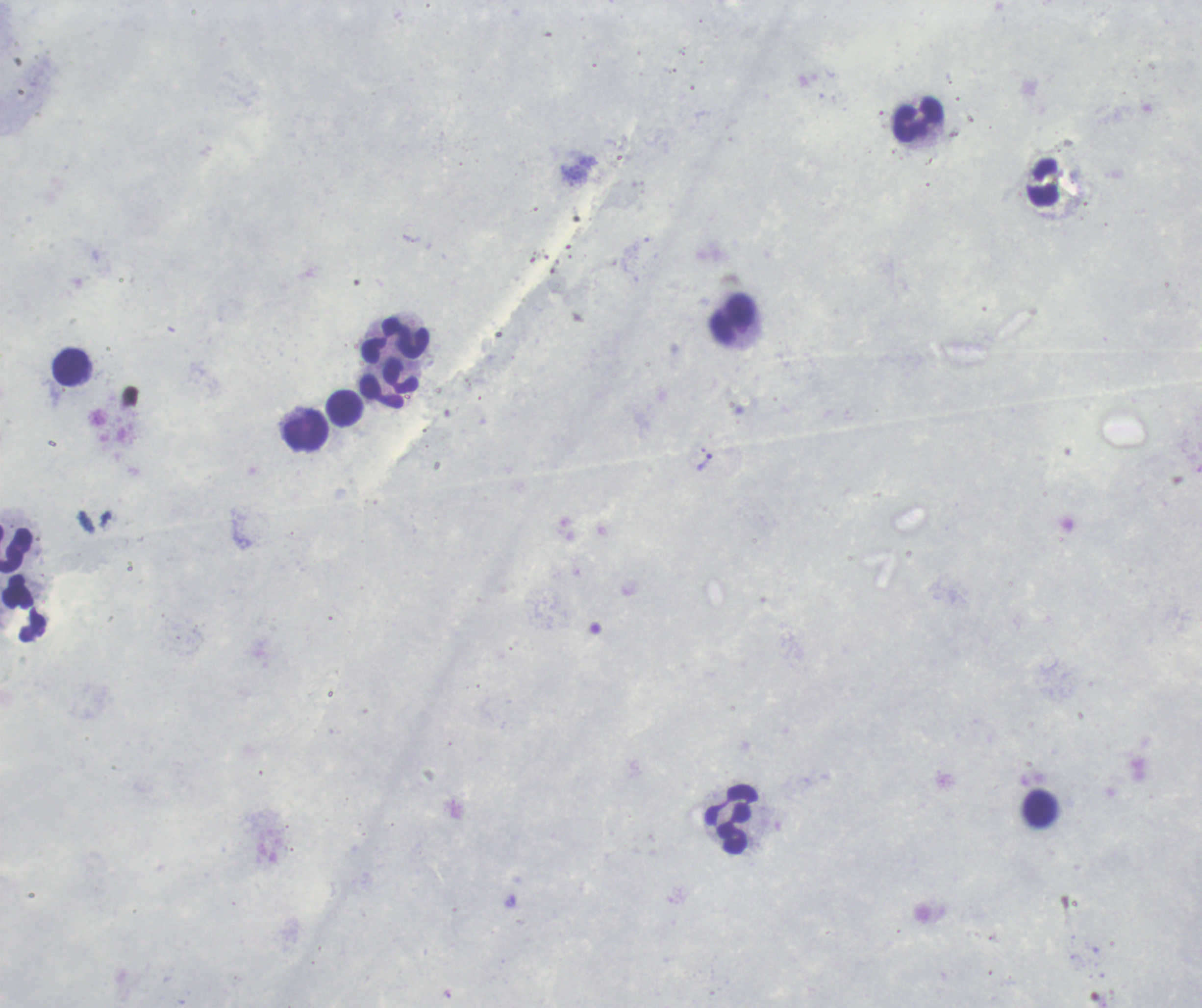

coordinate format = approximate centers as [x, y] in pixels
trophozoite locations = [704, 463]
leukocyte locations = [918, 121], [1044, 183], [732, 320], [396, 341], [70, 368], [401, 378], [381, 392], [344, 410], [306, 432], [16, 550], [23, 608], [1040, 809], [730, 820]
preparation = thick smear of blood
result = malaria parasites detected
background quality = poor
context = previously used in an actual diagnosis
magnification = 100x
field of view = one from this slide
image size = 1202×1008 pixels
stain = Romanowsky